Assess this cell for malaria.
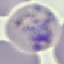

It is parasitized.

capture = smartphone through the microscope eyepiece
stain = Giemsa
image type = cell patch, automatically extracted from a larger field of view and resized to 64 × 64 pixels
preparation = thin smear